Locate every blood parasite and identify its species.
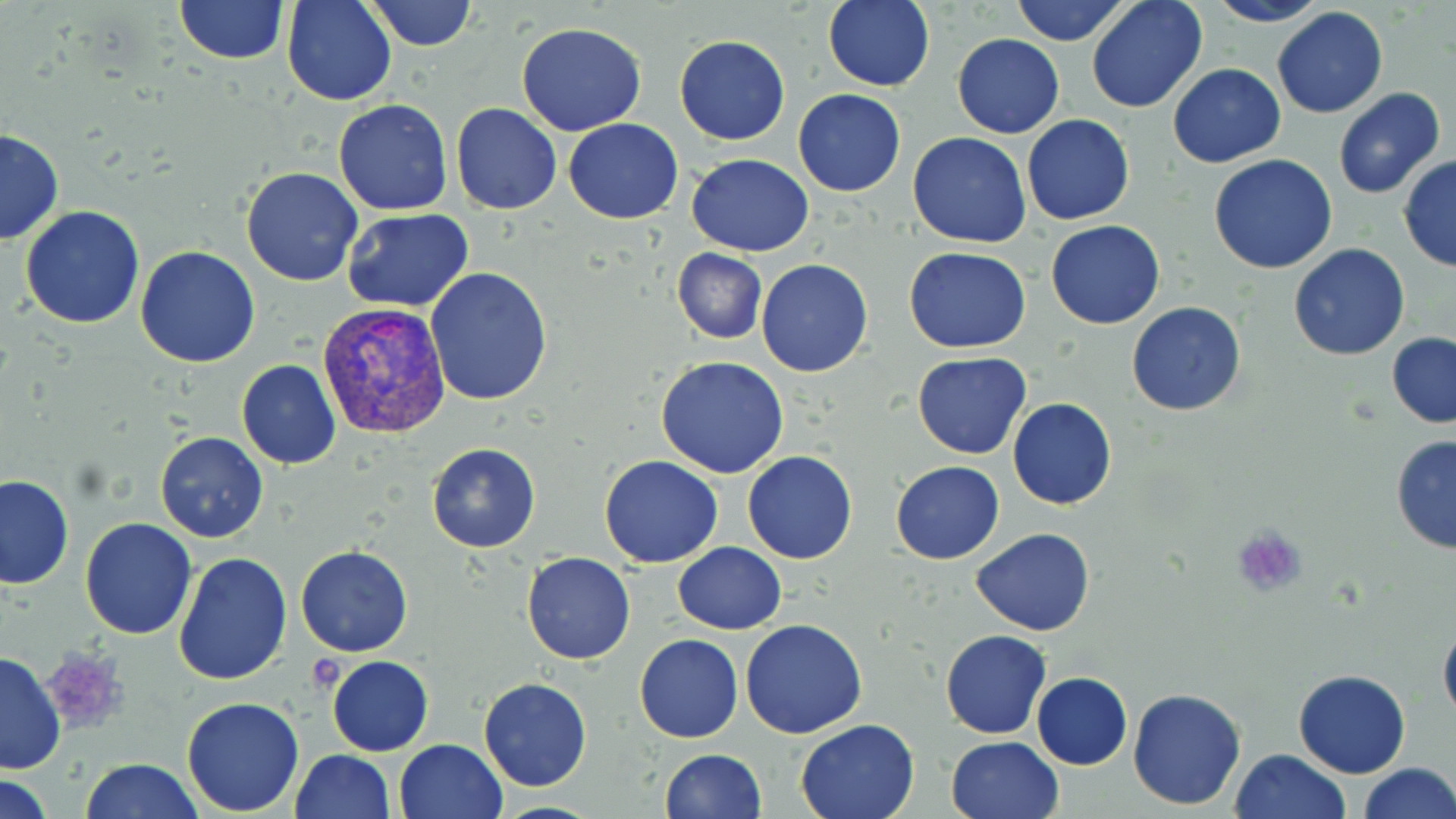
Approximate bounding boxes as (x1, y1, x2, y2) in pixels.
Plasmodium vivax-infected red blood cells: (316, 301, 452, 439).
No Plasmodium falciparum, Plasmodium ovale, Plasmodium malariae, Babesia divergens, or Trypanosoma brucei observed.

Platelet locations: (1232, 525, 1310, 599), (38, 649, 128, 737). Uninfected red blood cell locations: (172, 0, 289, 65), (282, 0, 396, 106), (366, 0, 474, 50), (823, 0, 935, 91), (1011, 0, 1129, 46), (1086, 0, 1209, 114), (1203, 0, 1331, 27), (1272, 6, 1388, 120), (515, 22, 648, 136), (951, 33, 1065, 139), (674, 35, 790, 145), (1168, 63, 1285, 166), (1333, 87, 1446, 199), (793, 88, 907, 196), (334, 99, 453, 216), (451, 103, 562, 215), (1022, 115, 1135, 225), (564, 119, 683, 223), (0, 128, 63, 246), (907, 131, 1031, 248), (686, 153, 814, 256), (1209, 155, 1339, 274), (1398, 156, 1456, 271), (240, 167, 363, 286), (20, 206, 146, 330), (342, 208, 475, 311), (1046, 219, 1164, 329), (1288, 242, 1410, 360), (135, 245, 259, 367), (902, 246, 1032, 353), (671, 249, 768, 343), (755, 259, 874, 377), (425, 267, 552, 406), (1127, 302, 1248, 417), (1387, 332, 1456, 428), (913, 352, 1030, 458), (655, 357, 790, 478), (237, 359, 341, 469), (1007, 397, 1117, 510), (155, 432, 269, 543), (1390, 434, 1456, 554), (425, 443, 541, 552), (743, 451, 857, 563), (600, 455, 723, 567), (890, 461, 1004, 565), (0, 474, 74, 590), (80, 518, 198, 639), (972, 527, 1094, 637), (673, 541, 786, 634), (296, 545, 413, 657), (172, 551, 292, 687), (521, 552, 636, 665), (1438, 617, 1456, 728), (741, 619, 867, 738), (940, 630, 1051, 738), (635, 634, 743, 742), (0, 651, 66, 775), (327, 655, 434, 756), (1293, 669, 1410, 778), (1031, 671, 1132, 770), (478, 677, 591, 791), (1127, 686, 1248, 811), (181, 696, 306, 815), (794, 717, 919, 819), (946, 735, 1063, 819), (392, 739, 508, 819), (658, 749, 766, 819), (1229, 749, 1348, 819), (289, 750, 395, 819), (79, 758, 205, 819), (1356, 763, 1455, 819), (2, 775, 57, 819), (491, 799, 607, 818). Slide-level diagnosis: Plasmodium vivax. Image is 1456×819 pixels. Single field of view. May-Grünwald-Giemsa-stained preparation. Captured at 1000x magnification. Light microscopy. Thin blood film.